Name the parasite shown.
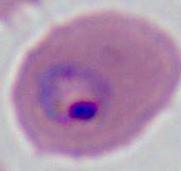
Plasmodium.

Micrograph. 400x or 1000x magnification.